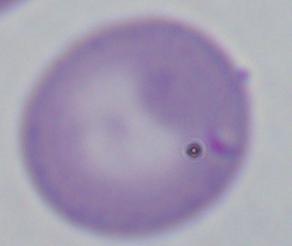

modality = micrograph
magnification = 1000x
identification = Babesia